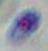
Summary:
  - Magnification: 1000x
  - Modality: micrograph
  - Identification: Toxoplasma gondii